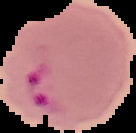
Cell region segmented out of the field of view; the surrounding area is masked to black. Image is 136×133 pixels. Malaria status: parasitized. From a thin blood smear.